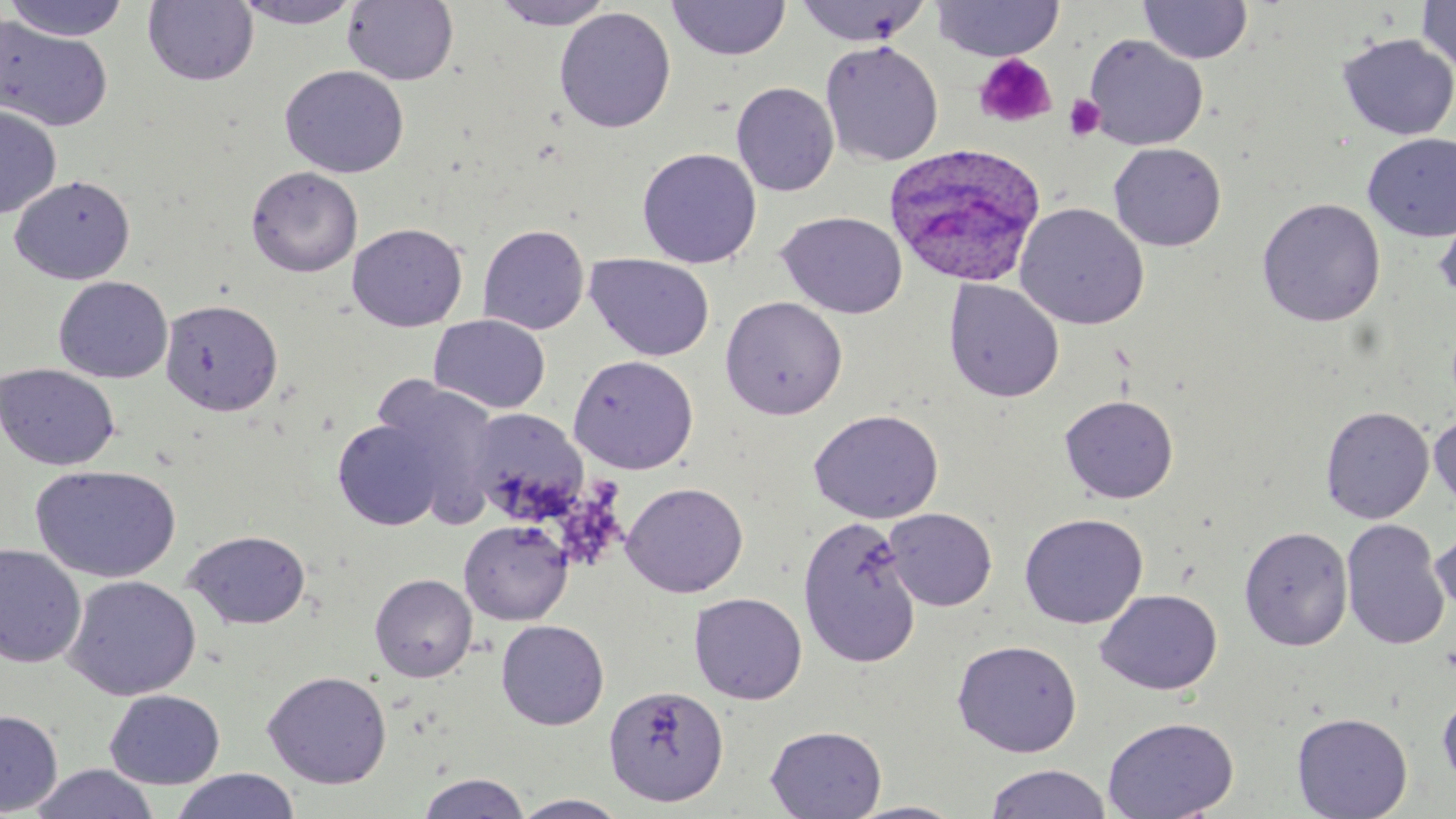 Approximate bounding boxes as (x1,y1)-(x2,y2) corner pairs in pixels. Uninfected red blood cell locations: (5,0)-(133,41), (143,0)-(259,87), (231,0)-(365,29), (491,0)-(615,29), (931,0)-(1063,61), (343,1)-(458,85), (667,1)-(791,61), (793,1)-(932,47), (1139,1)-(1253,65), (1416,1)-(1456,74), (554,6)-(676,133), (0,15)-(114,133), (1337,33)-(1456,141), (1084,34)-(1208,151), (820,40)-(944,166), (280,65)-(409,178), (731,81)-(840,197), (0,105)-(61,219), (1363,133)-(1456,241), (1108,142)-(1227,252), (637,147)-(762,269), (245,166)-(363,277), (9,174)-(135,285), (1257,197)-(1386,327), (1434,201)-(1456,307), (1014,202)-(1150,330), (777,211)-(908,319), (347,223)-(468,332), (477,223)-(590,335), (585,253)-(716,362), (53,276)-(173,383), (943,278)-(1065,403), (720,296)-(848,420), (160,298)-(284,416), (428,314)-(551,414), (567,353)-(700,474), (1,363)-(121,471), (373,378)-(502,523), (1059,394)-(1179,504), (1320,405)-(1435,524), (808,408)-(944,524), (485,409)-(584,523), (1429,410)-(1456,516), (332,418)-(445,530), (30,464)-(181,583), (621,481)-(748,598), (884,508)-(997,611), (1019,512)-(1148,629), (797,515)-(923,667), (459,519)-(573,625), (1340,519)-(1450,650), (1239,525)-(1353,651), (1430,525)-(1456,622), (183,528)-(312,630), (0,543)-(87,669), (369,573)-(477,682), (63,574)-(201,701), (1095,588)-(1223,695), (689,592)-(808,704), (495,619)-(609,730), (952,638)-(1082,757), (262,670)-(393,789), (603,684)-(729,806), (104,689)-(226,789), (1438,690)-(1456,793), (0,709)-(63,816), (1291,712)-(1413,819), (1102,716)-(1240,819), (765,725)-(886,818), (29,764)-(161,819), (983,764)-(1113,819), (169,769)-(301,819), (415,772)-(532,819), (511,793)-(631,818), (844,801)-(968,818). Platelet locations: (973,54)-(1057,129), (1063,94)-(1106,141). Plasmodium ovale-infected red blood cell locations: (882,141)-(1047,287). Slide-level diagnosis: Plasmodium ovale. Captured at 1000x magnification. Image is 1456×819 pixels. Optical microscopy. May-Grünwald-Giemsa stain. One field of a larger specimen. Thin blood film.